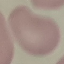
Result: no malaria parasites detected. Giemsa stain. Cell patch, automatically extracted from a larger field of view and resized to 64 × 64 pixels. Photographed with a smartphone camera at the microscope eyepiece. Thin smear of blood.